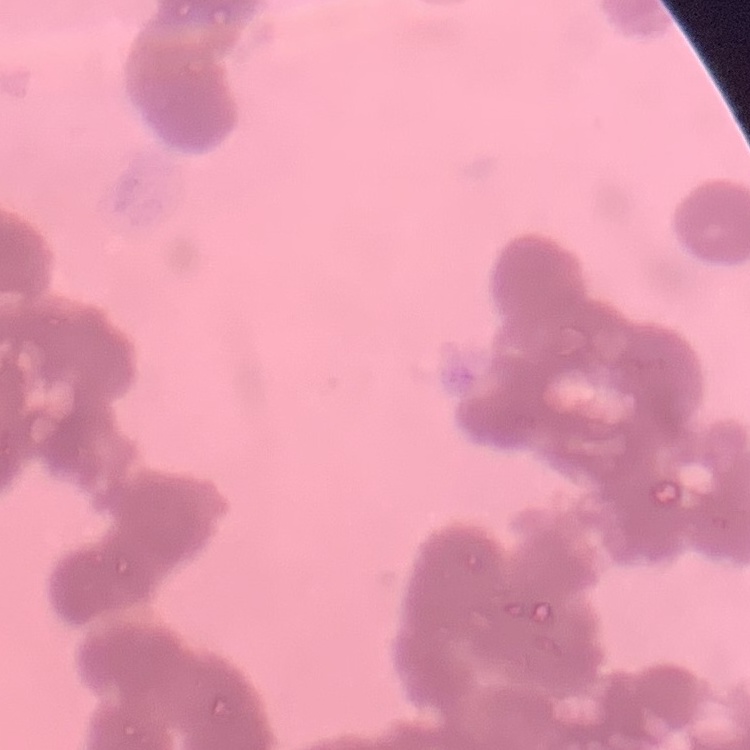
erythrocyte morphology = rouleaux formation
preparation = thin blood film
image type = square crop of a larger photomicrograph
stain = Field's or Giemsa